Report the malaria status of this cell.
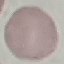

It is uninfected.

capture = smartphone through the microscope eyepiece
preparation = thin smear
image type = cell patch, automatically extracted from a larger field of view and resized to 64 × 64 pixels
stain = Giemsa